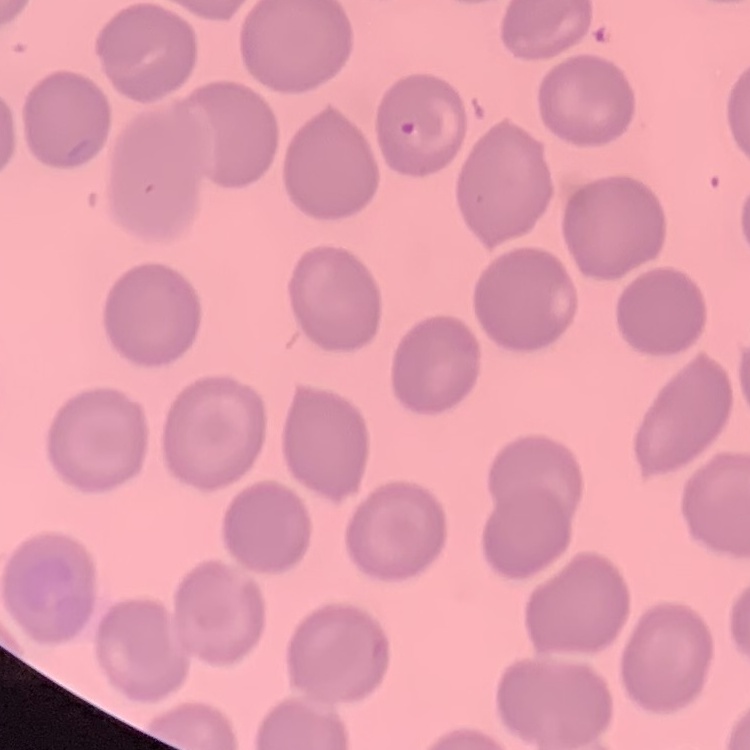 The red blood cells show no rouleaux formation. Stained with either Field's or Giemsa. Thin blood smear. Square crop of a larger photomicrograph.